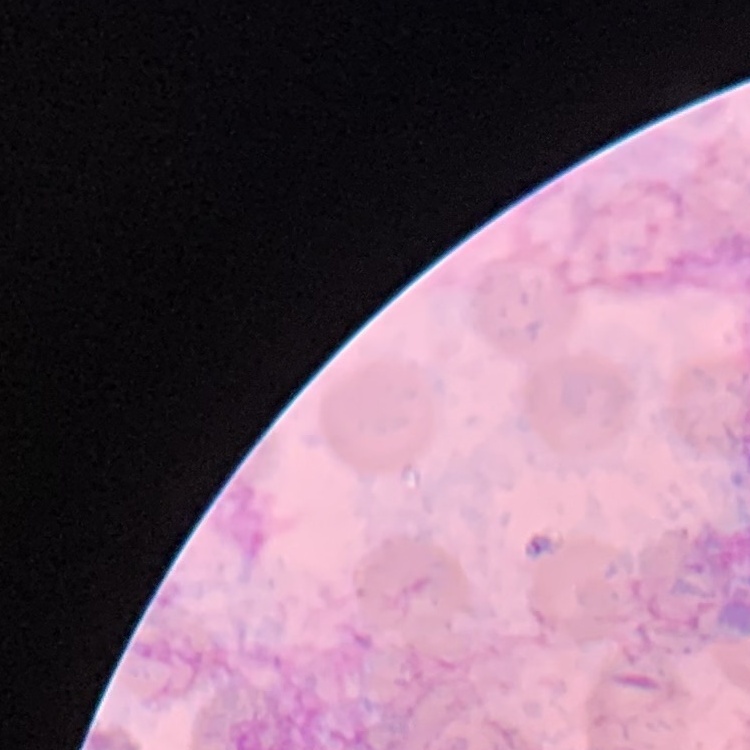

red blood cell morphology = no rouleaux formation
image type = square crop of a larger photomicrograph
stain = Field's or Giemsa
preparation = thin blood film